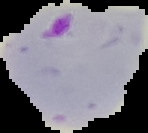
Malaria status: parasitized. Image is 148×133 pixels. Segmented cell region on a black background. From a thin blood smear.